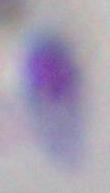

1000x magnification. Micrograph. Toxoplasma gondii is shown.